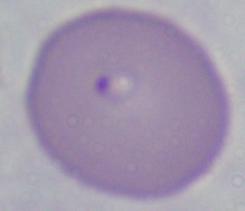
Summary:
  - Identification: Babesia
  - Magnification: 1000x
  - Modality: photomicrograph